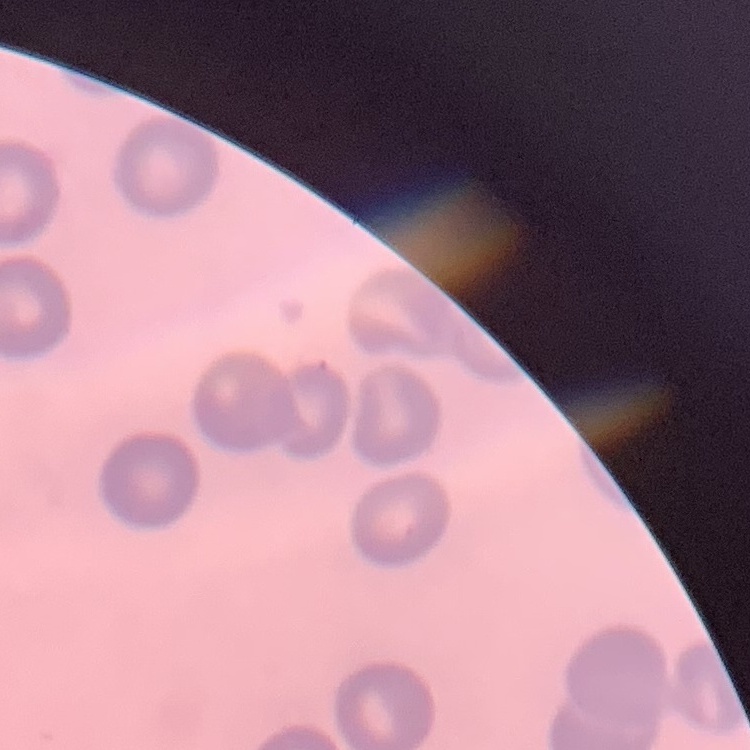

erythrocyte_morphology: no rouleaux formation
stain: Field's or Giemsa
image_type: one tile cut from a larger photomicrograph
preparation: thin peripheral smear